Outline each Plasmodium malariae-infected red blood cell.
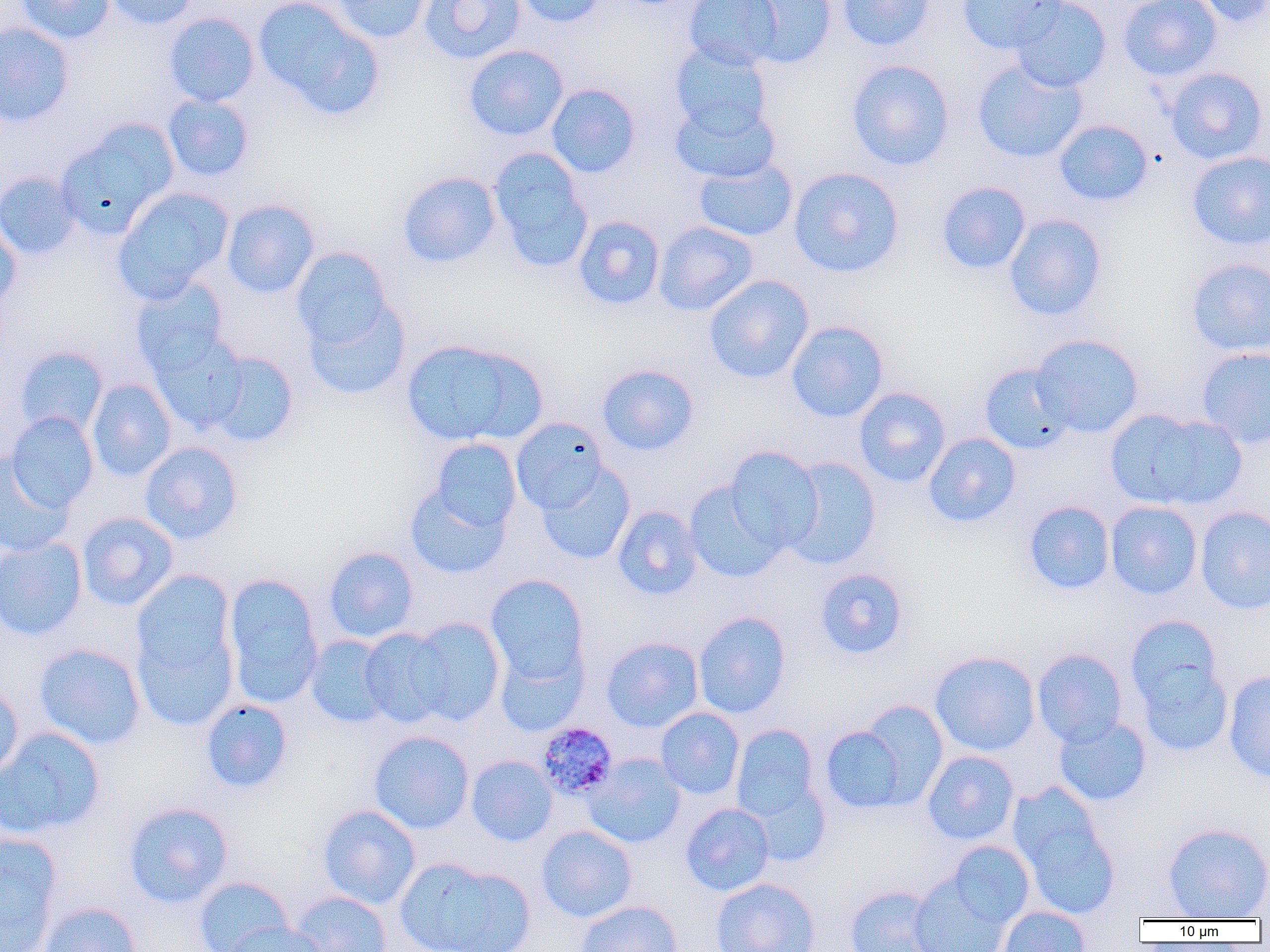

Approximate bounding boxes as [x1, y1, x2, y2] in pixels.
Plasmodium malariae-infected red blood cells: [536, 721, 618, 801].

{
  "slide_level_diagnosis": "Plasmodium malariae",
  "image_size": "1270×952 pixels",
  "field_of_view": "one of a larger specimen",
  "magnification": "1000x",
  "uninfected_red_blood_cell_locations": "approximate bounding boxes as [x1, y1, x2, y2] in pixels: [14, 0, 115, 44], [104, 0, 200, 30], [253, 0, 381, 117], [330, 0, 431, 43], [418, 0, 525, 64], [514, 0, 608, 28], [684, 0, 783, 70], [837, 0, 935, 51], [957, 0, 1065, 53], [1009, 0, 1112, 92], [1119, 0, 1222, 80], [1189, 0, 1270, 28], [740, 1, 837, 69], [163, 13, 260, 107], [0, 23, 73, 127], [669, 42, 772, 138], [463, 44, 569, 141], [846, 59, 954, 170], [972, 59, 1088, 163], [1164, 67, 1268, 165], [546, 84, 640, 178], [162, 94, 254, 182], [670, 98, 780, 184], [1053, 119, 1153, 207], [55, 122, 178, 239], [488, 149, 593, 271], [1186, 151, 1270, 250], [693, 156, 798, 242], [788, 167, 905, 277], [397, 171, 502, 268], [0, 172, 81, 260], [937, 181, 1031, 274], [112, 187, 233, 303], [221, 199, 320, 298], [1003, 214, 1107, 321], [573, 215, 665, 310], [0, 220, 21, 310], [653, 221, 757, 316], [291, 247, 394, 349], [1185, 258, 1270, 357], [704, 275, 814, 383], [130, 278, 229, 375], [302, 296, 410, 400], [786, 320, 889, 422], [149, 331, 249, 434], [1031, 334, 1144, 438], [401, 338, 545, 448], [15, 346, 108, 436], [1196, 346, 1270, 449], [205, 351, 299, 448], [597, 364, 699, 455], [979, 364, 1076, 454], [87, 379, 177, 481], [854, 387, 951, 487], [1105, 408, 1244, 512], [6, 412, 99, 513], [510, 418, 609, 514], [923, 433, 1021, 527], [429, 438, 522, 534], [140, 442, 242, 544], [724, 446, 823, 553], [0, 453, 74, 557], [783, 457, 882, 570], [536, 463, 636, 565], [684, 482, 785, 583], [404, 483, 510, 579], [1023, 500, 1115, 595], [1105, 501, 1202, 600], [612, 505, 703, 600], [1195, 506, 1270, 615], [77, 512, 178, 611], [0, 536, 88, 640], [323, 546, 418, 643], [815, 568, 907, 658], [131, 570, 235, 677], [223, 574, 323, 706], [486, 574, 589, 685], [693, 611, 791, 718], [1125, 615, 1222, 708], [406, 617, 506, 726], [132, 625, 237, 731], [359, 627, 454, 727], [304, 636, 393, 728], [601, 637, 703, 732], [494, 642, 588, 737], [34, 643, 146, 750], [1032, 649, 1128, 746], [930, 651, 1040, 756], [1135, 659, 1234, 757], [1223, 670, 1270, 783], [0, 684, 24, 782], [201, 698, 293, 794], [853, 700, 949, 808], [655, 707, 745, 800], [1053, 716, 1152, 806], [820, 723, 913, 814], [730, 724, 821, 824], [0, 726, 106, 840], [369, 731, 474, 834], [922, 750, 1019, 845], [583, 753, 687, 848], [465, 755, 557, 847], [746, 780, 832, 867], [1011, 792, 1120, 919], [123, 802, 233, 908], [680, 803, 774, 897], [317, 805, 420, 909], [1162, 822, 1270, 920], [536, 825, 636, 922], [0, 833, 61, 951], [946, 840, 1035, 928], [395, 858, 532, 952], [909, 875, 1011, 952], [193, 876, 293, 952], [710, 877, 820, 952], [844, 886, 944, 952], [289, 891, 391, 952], [576, 900, 683, 952], [36, 902, 141, 952], [996, 905, 1091, 952], [223, 922, 327, 952]",
  "modality": "light microscopy",
  "preparation": "thin blood film"
}